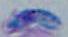
Micrograph. Captured at 1000x magnification. Toxoplasma gondii is seen.